Name the parasite shown.
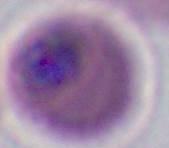
Plasmodium.

magnification: 400x or 1000x
modality: micrograph